Locate and identify every blood parasite.
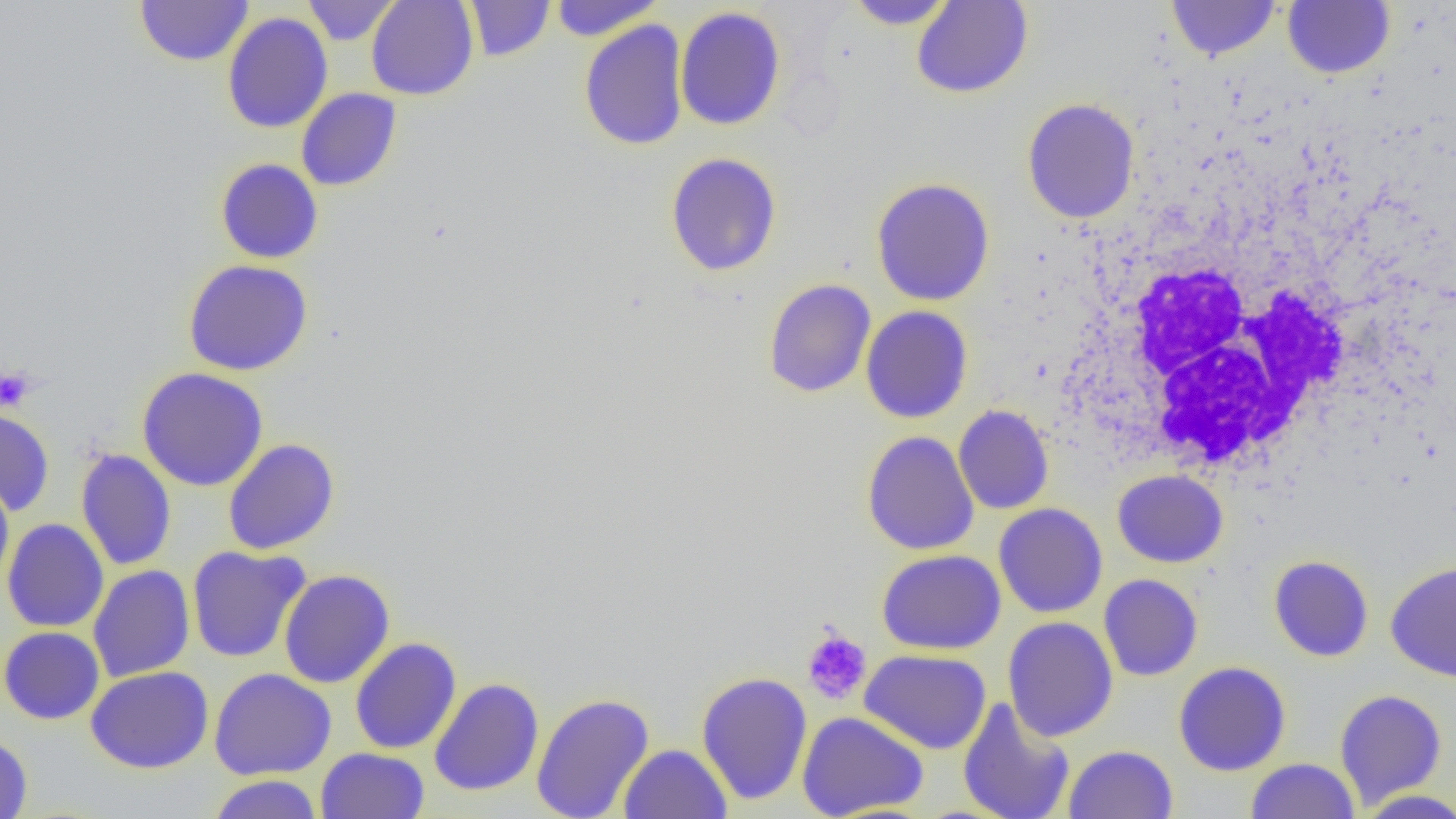
No blood parasites observed.

Approximate bounding boxes as (x1,y1)-(x2,y2) corner pairs in pixels. White blood cell locations: (1079,245)-(1352,476). Uninfected red blood cell locations: (135,0)-(254,67), (302,0)-(401,45), (366,0)-(479,100), (549,0)-(664,40), (844,0)-(957,30), (911,0)-(1033,99), (1167,0)-(1280,61), (464,1)-(555,61), (1283,1)-(1396,79), (674,6)-(787,131), (222,12)-(333,133), (579,19)-(689,151), (296,88)-(402,191), (1022,98)-(1140,223), (665,152)-(782,277), (215,158)-(323,264), (870,177)-(995,306), (183,259)-(313,376), (763,278)-(877,398), (860,305)-(973,424), (137,367)-(269,491), (953,405)-(1054,514), (0,407)-(55,516), (862,430)-(979,555), (222,438)-(340,556), (76,449)-(176,571), (1113,469)-(1228,568), (0,474)-(14,591), (993,503)-(1108,618), (1,518)-(109,633), (186,545)-(311,663), (877,549)-(1006,655), (1268,555)-(1374,662), (1385,561)-(1456,683), (88,564)-(195,682), (279,569)-(395,688), (1098,574)-(1203,681), (1003,616)-(1118,741), (1,626)-(105,725), (350,637)-(462,754), (860,649)-(991,755), (1173,661)-(1291,776), (85,666)-(214,773), (209,668)-(336,779), (696,671)-(812,806), (429,677)-(544,796), (1334,689)-(1448,808), (531,693)-(653,819), (958,698)-(1075,819), (797,710)-(929,818), (0,732)-(33,819), (618,744)-(732,819), (1063,744)-(1178,819), (316,747)-(429,819), (1245,758)-(1360,819), (208,774)-(323,818), (1354,788)-(1456,818). Platelet locations: (0,367)-(35,413), (802,629)-(872,705). Slide-level diagnosis: no evidence of blood parasites. Single field of view. Light microscopy. 1000x magnification. Image is 1456×819 pixels. Thin blood smear.